Assess the morphology of the red blood cells.
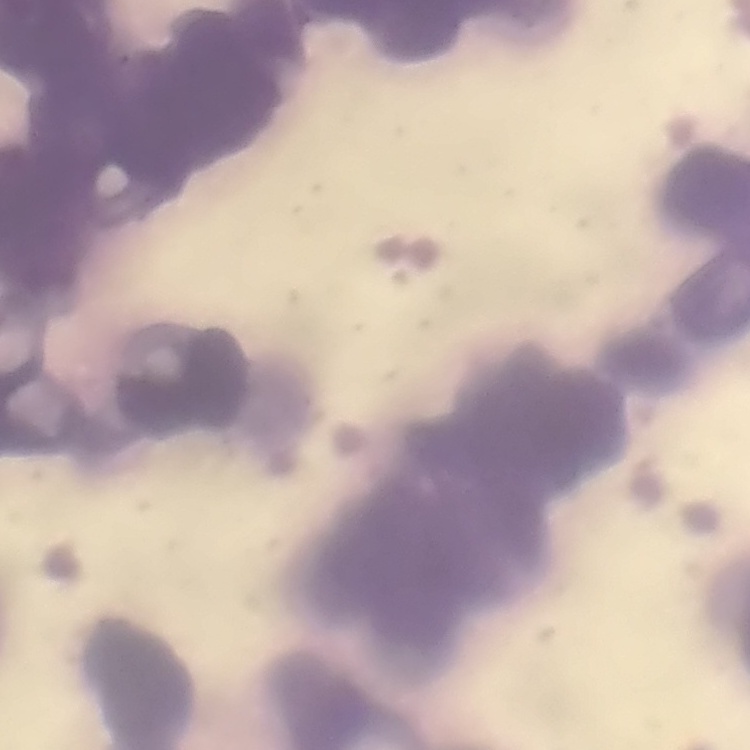
They show rouleaux formation.

stain = Field's or Giemsa
preparation = thin blood film
image type = square crop of a larger photomicrograph